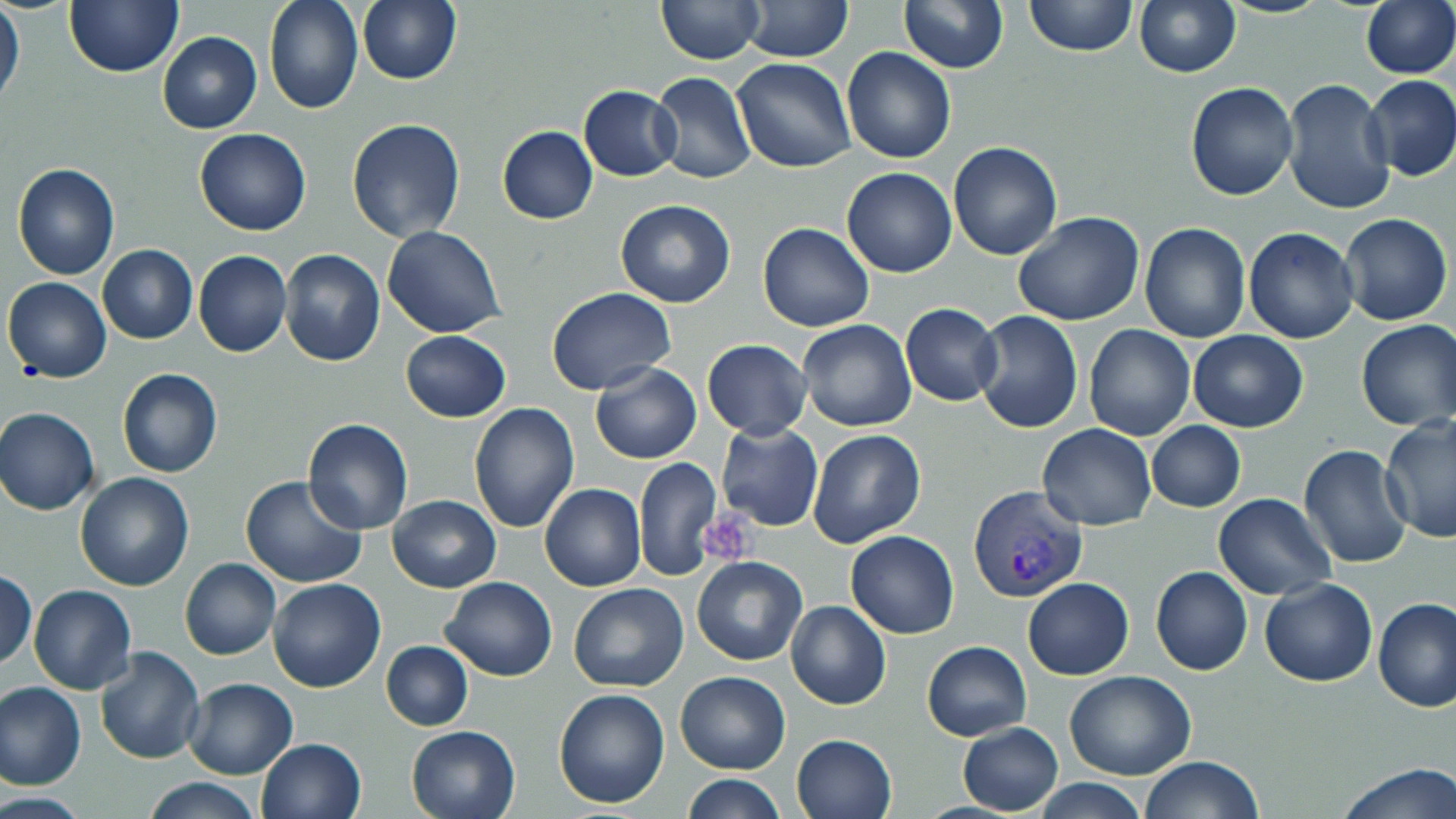

slide-level diagnosis = Plasmodium vivax
field of view = single
image size = 1456×819 pixels
Plasmodium vivax-infected red blood cell locations = approximate bounding boxes as named x1/y1/x2/y2 corners in pixels: (x1=968, y1=485, x2=1088, y2=603)
platelet locations = approximate bounding boxes as named x1/y1/x2/y2 corners in pixels: (x1=696, y1=516, x2=758, y2=566)
preparation = thin blood film
magnification = 1000x
modality = optical microscopy
stain = May-Grünwald-Giemsa
uninfected red blood cell locations = approximate bounding boxes as named x1/y1/x2/y2 corners in pixels: (x1=65, y1=0, x2=183, y2=77), (x1=263, y1=0, x2=363, y2=115), (x1=357, y1=0, x2=462, y2=86), (x1=658, y1=0, x2=762, y2=64), (x1=1134, y1=0, x2=1241, y2=77), (x1=1358, y1=0, x2=1456, y2=80), (x1=737, y1=1, x2=852, y2=61), (x1=899, y1=1, x2=1009, y2=73), (x1=1022, y1=1, x2=1138, y2=56), (x1=0, y1=2, x2=25, y2=109), (x1=157, y1=32, x2=263, y2=134), (x1=841, y1=47, x2=957, y2=164), (x1=732, y1=57, x2=856, y2=172), (x1=649, y1=73, x2=756, y2=185), (x1=1361, y1=75, x2=1456, y2=182), (x1=1281, y1=79, x2=1396, y2=215), (x1=1185, y1=82, x2=1298, y2=200), (x1=579, y1=86, x2=682, y2=180), (x1=346, y1=118, x2=466, y2=243), (x1=496, y1=125, x2=598, y2=224), (x1=193, y1=129, x2=310, y2=235), (x1=947, y1=141, x2=1064, y2=259), (x1=11, y1=162, x2=120, y2=280), (x1=842, y1=168, x2=957, y2=278), (x1=615, y1=200, x2=737, y2=308), (x1=1013, y1=212, x2=1144, y2=326), (x1=1338, y1=212, x2=1452, y2=325), (x1=1139, y1=222, x2=1251, y2=343), (x1=756, y1=223, x2=874, y2=332), (x1=382, y1=226, x2=506, y2=339), (x1=1244, y1=227, x2=1360, y2=344), (x1=98, y1=245, x2=198, y2=344), (x1=279, y1=249, x2=386, y2=366), (x1=194, y1=250, x2=291, y2=359), (x1=2, y1=276, x2=113, y2=384), (x1=547, y1=288, x2=676, y2=396), (x1=901, y1=303, x2=1002, y2=404), (x1=972, y1=311, x2=1084, y2=434), (x1=1355, y1=319, x2=1456, y2=431), (x1=797, y1=320, x2=917, y2=430), (x1=1083, y1=324, x2=1194, y2=441), (x1=1186, y1=329, x2=1308, y2=432), (x1=400, y1=330, x2=511, y2=421), (x1=701, y1=339, x2=812, y2=440), (x1=590, y1=361, x2=703, y2=465), (x1=116, y1=368, x2=223, y2=478), (x1=468, y1=405, x2=580, y2=533), (x1=1, y1=408, x2=100, y2=516), (x1=1379, y1=416, x2=1456, y2=544), (x1=302, y1=418, x2=413, y2=535), (x1=716, y1=421, x2=823, y2=532), (x1=1146, y1=421, x2=1246, y2=512), (x1=1038, y1=423, x2=1157, y2=530), (x1=807, y1=428, x2=928, y2=549), (x1=1298, y1=444, x2=1413, y2=569), (x1=634, y1=456, x2=720, y2=580), (x1=74, y1=473, x2=196, y2=591), (x1=241, y1=477, x2=366, y2=588), (x1=539, y1=483, x2=646, y2=591), (x1=1213, y1=494, x2=1336, y2=601), (x1=388, y1=495, x2=501, y2=592), (x1=845, y1=530, x2=960, y2=639), (x1=692, y1=556, x2=806, y2=666), (x1=180, y1=558, x2=280, y2=660), (x1=1150, y1=566, x2=1253, y2=676), (x1=1, y1=568, x2=38, y2=670), (x1=267, y1=577, x2=386, y2=693), (x1=439, y1=577, x2=558, y2=681), (x1=1023, y1=577, x2=1134, y2=679), (x1=1259, y1=579, x2=1378, y2=688), (x1=568, y1=582, x2=689, y2=692), (x1=27, y1=584, x2=137, y2=694), (x1=1373, y1=597, x2=1455, y2=713), (x1=787, y1=601, x2=891, y2=710), (x1=922, y1=640, x2=1031, y2=741), (x1=381, y1=641, x2=474, y2=731), (x1=94, y1=647, x2=205, y2=764), (x1=1065, y1=670, x2=1197, y2=780), (x1=676, y1=671, x2=790, y2=774), (x1=182, y1=678, x2=299, y2=780), (x1=0, y1=681, x2=85, y2=791), (x1=553, y1=688, x2=669, y2=807), (x1=405, y1=723, x2=521, y2=819), (x1=956, y1=723, x2=1063, y2=815), (x1=790, y1=733, x2=897, y2=819), (x1=255, y1=737, x2=366, y2=819), (x1=1139, y1=756, x2=1265, y2=818), (x1=1336, y1=761, x2=1455, y2=818), (x1=681, y1=775, x2=788, y2=818), (x1=140, y1=777, x2=263, y2=818), (x1=1030, y1=779, x2=1151, y2=818)